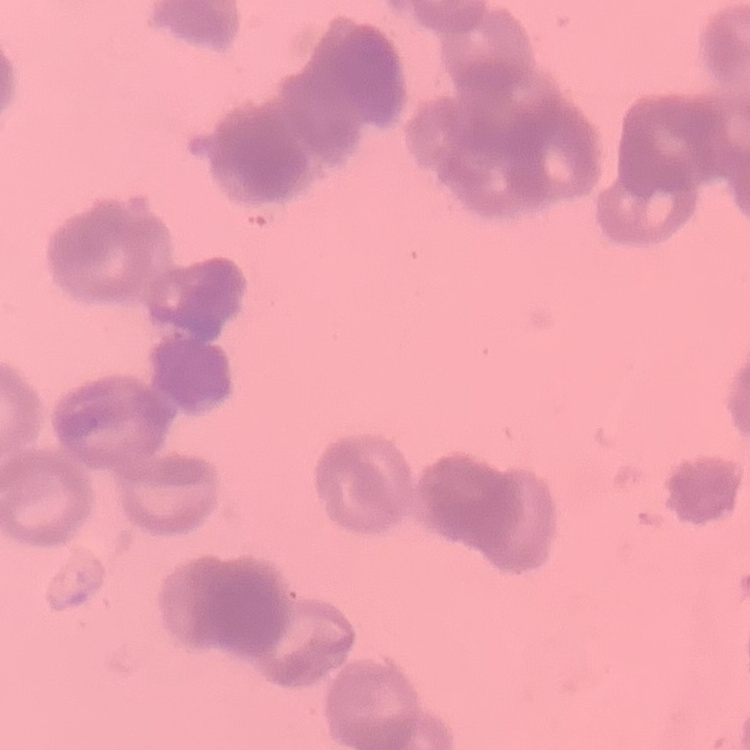
The erythrocytes show rouleaux formation. Square crop of a larger photomicrograph. Field's or Giemsa stain. Thin peripheral smear.